Name the parasite shown.
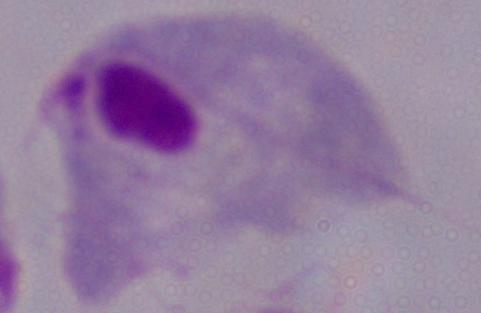

This is a trichomonad.

Summary:
  - Magnification: 1000x
  - Modality: photomicrograph